Classify this cell by malaria status.
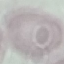
Uninfected.

stain = Giemsa
preparation = thin blood smear
image type = cell patch, automatically extracted from a larger field of view and resized to 64 × 64 pixels
capture = smartphone camera at the microscope eyepiece